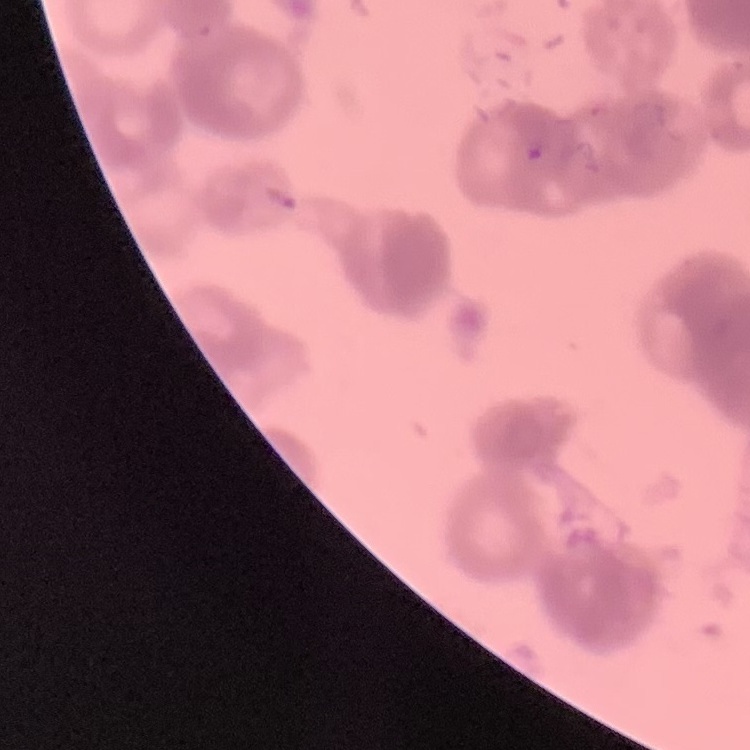
red blood cell morphology = rouleaux formation
stain = Field's or Giemsa
preparation = thin peripheral smear
image type = square crop of a larger photomicrograph